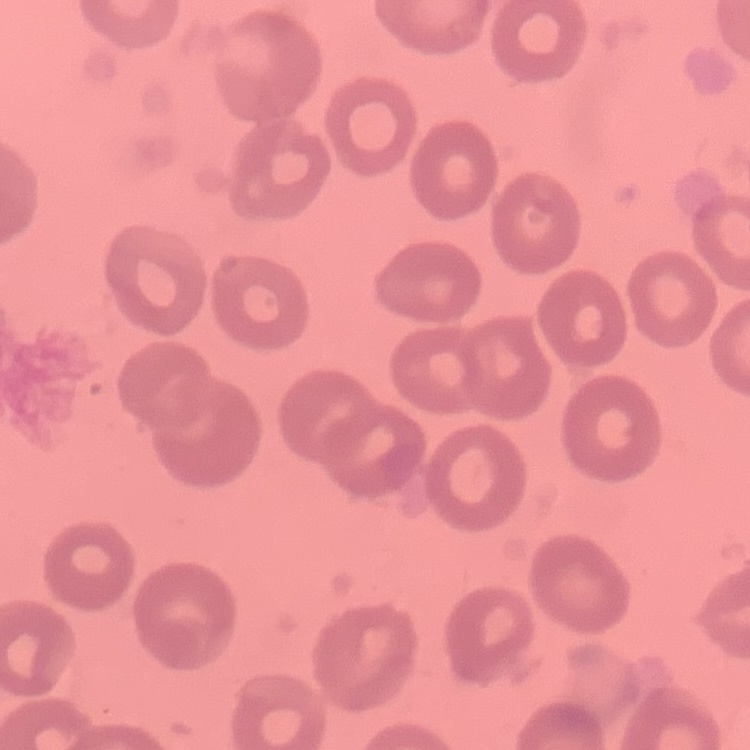

The erythrocytes show no rouleaux formation. One tile cut from a larger photomicrograph. Field's or Giemsa stain. Thin blood smear.